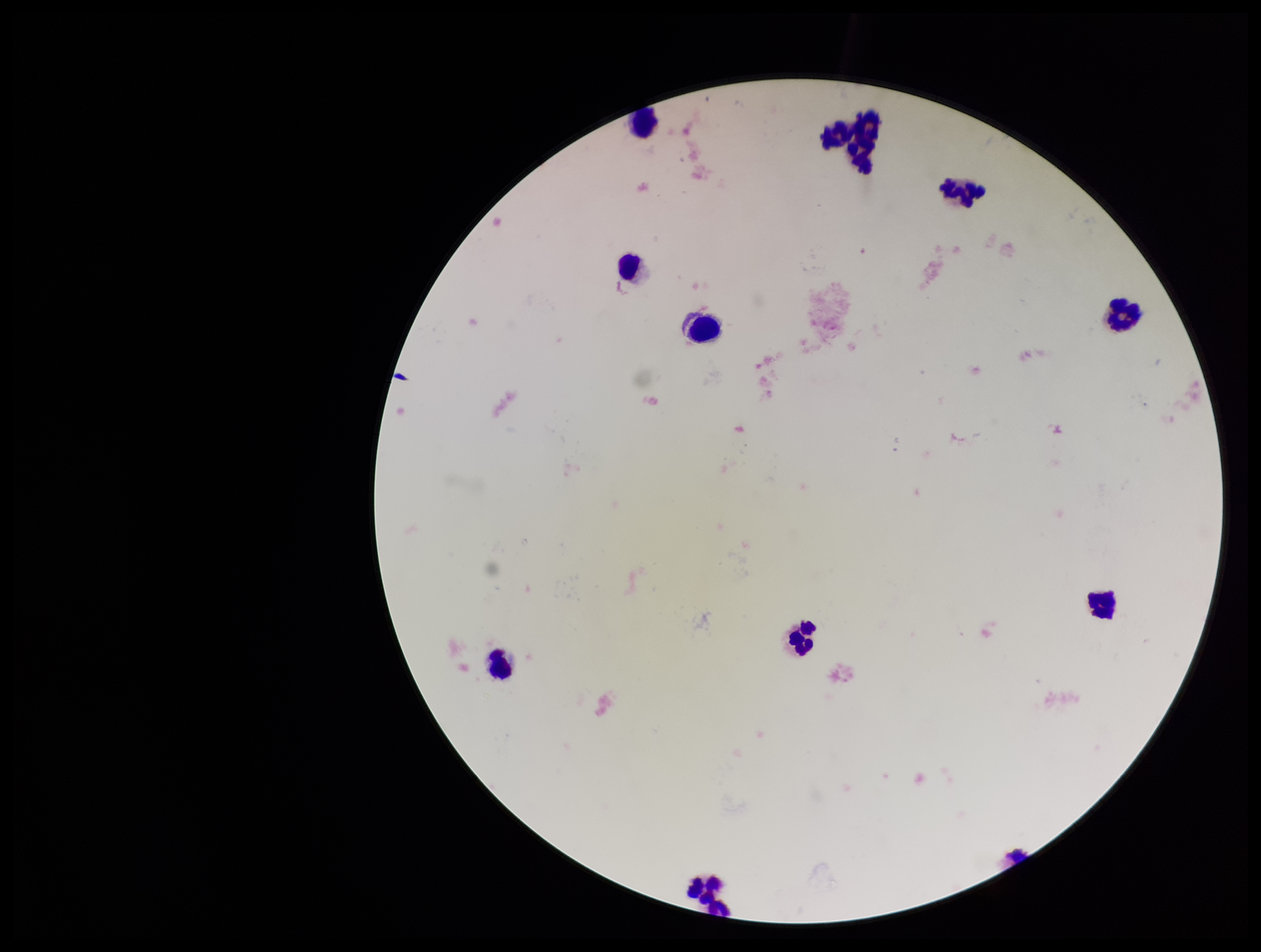

{
  "parasite_count": 0,
  "preparation": "thick smear",
  "stain": "Giemsa",
  "capture": "smartphone photograph through the microscope eyepiece",
  "image_size": "1261×952 pixels",
  "plasmodium_parasites": "none seen",
  "patient_malaria_status": "negative",
  "field_of_view": "one from this slide",
  "leukocyte_count": 12
}